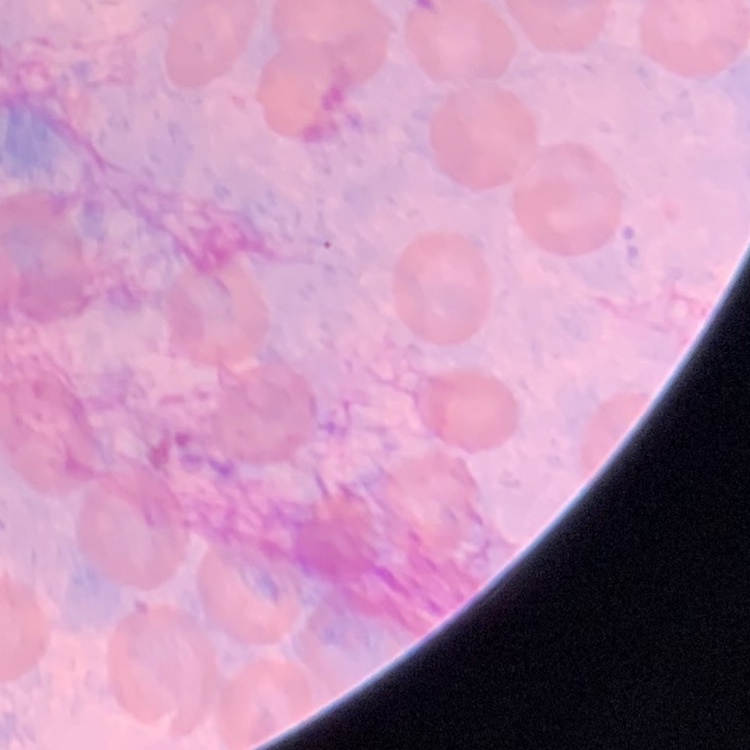

red blood cell morphology = no rouleaux formation
image type = square crop of a larger photomicrograph
preparation = thin blood smear
stain = Field's or Giemsa